Classify this cell by malaria status.
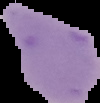

Uninfected.

Summary:
  - Image size: 100×103 pixels
  - Preparation: thin blood film
  - Image type: cell region segmented out of the field of view; surrounding area masked to black